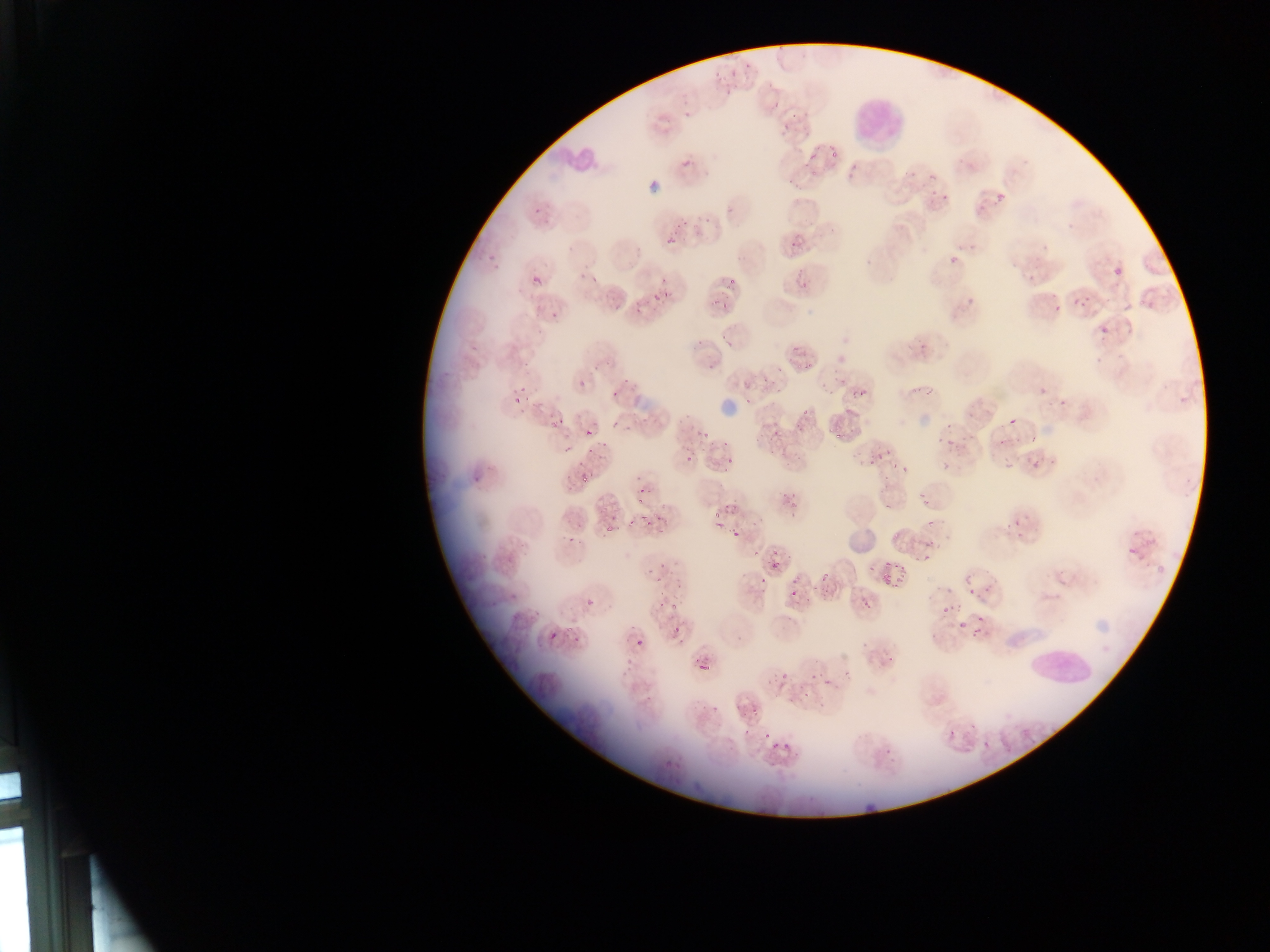

capture = mobile-phone photograph through a microscope
country = Ghana
malaria parasite locations = approximate bounding boxes as left top right bottom in pixels: 532 200 543 213; 666 234 677 248; 786 234 805 254; 486 246 500 263; 948 255 956 261; 1109 263 1129 284; 575 270 588 285; 1018 270 1035 280; 531 274 542 286; 655 274 670 287; 725 277 739 287; 649 283 673 302; 1069 293 1088 307; 718 294 737 309; 963 298 979 308; 1052 298 1064 309; 631 299 648 309; 544 305 561 318; 1093 318 1118 344; 621 369 635 384; 576 380 586 391; 851 380 873 399; 1036 381 1051 400; 607 384 619 399; 509 390 522 403; 743 395 756 405; 674 412 688 422; 1005 415 1022 430; 550 416 564 430; 612 416 622 432; 769 425 783 435; 700 426 714 437; 583 428 593 441; 935 432 963 446; 1025 433 1044 447; 559 447 571 455; 933 449 956 471; 868 450 891 464; 685 452 694 468; 725 455 737 465; 1034 455 1058 470; 1002 458 1022 472; 901 466 912 476; 576 468 593 484; 469 476 483 487; 916 488 935 514; 786 492 804 506; 1006 507 1028 526; 924 513 940 535; 717 516 727 529; 628 518 636 527; 732 529 742 540; 562 530 578 548; 922 538 940 560; 1121 538 1148 569; 754 545 764 560; 767 551 782 572; 898 561 915 594; 880 562 890 584; 818 566 831 583; 966 577 979 591; 760 578 767 586; 986 579 996 591; 789 586 805 600; 857 592 877 610; 583 594 595 605; 937 599 956 621; 975 609 985 639; 956 611 970 633; 547 630 560 645; 634 637 647 650
field of view = single
preparation = thin blood film
image size = 1270×952 pixels
leukocyte locations = approximate bounding boxes as left top right bottom in pixels: 851 87 908 153; 1022 639 1096 691